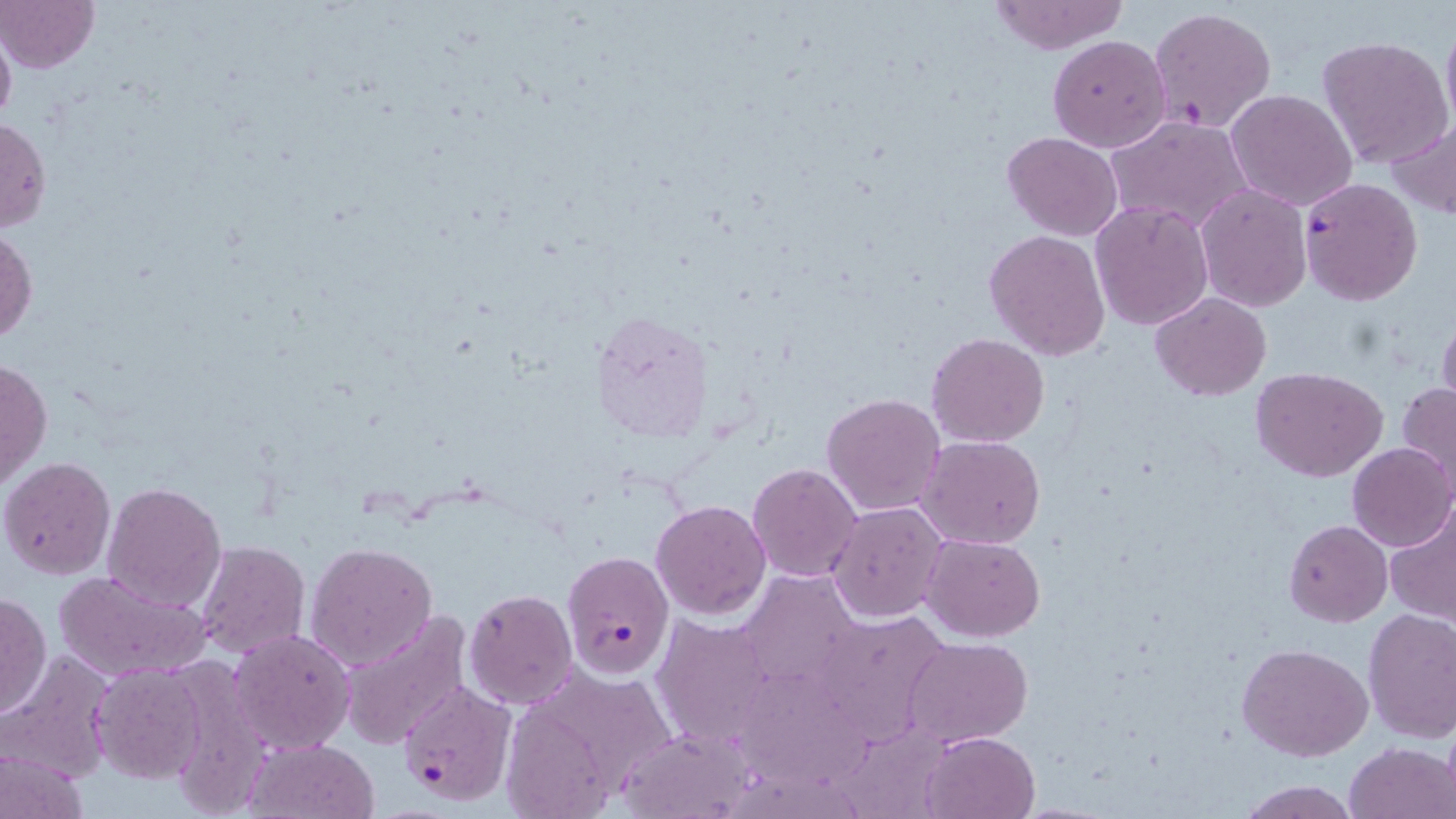

Approximate bounding boxes as (x1, y1, x2, y2) in pixels. Plasmodium falciparum-infected red blood cell locations: (1297, 177, 1422, 305), (562, 549, 675, 680), (396, 681, 519, 806). Uninfected red blood cell locations: (0, 0, 99, 72), (987, 1, 1129, 54), (1148, 7, 1276, 136), (1440, 9, 1456, 138), (0, 17, 16, 138), (1048, 34, 1171, 154), (1317, 35, 1453, 170), (1228, 89, 1357, 212), (1104, 116, 1252, 235), (0, 117, 52, 235), (1388, 117, 1456, 220), (1002, 131, 1124, 239), (1195, 185, 1312, 312), (1090, 201, 1213, 330), (1, 227, 38, 346), (984, 228, 1111, 363), (1150, 291, 1272, 402), (1437, 308, 1456, 422), (590, 312, 709, 443), (926, 333, 1050, 447), (1, 356, 52, 491), (1251, 367, 1388, 481), (1397, 382, 1456, 500), (821, 392, 946, 515), (918, 436, 1047, 550), (1346, 442, 1455, 553), (1, 456, 116, 580), (747, 463, 862, 583), (101, 481, 228, 614), (652, 499, 771, 620), (828, 502, 947, 621), (1383, 502, 1456, 628), (1285, 519, 1393, 626), (923, 533, 1045, 641), (305, 540, 437, 670), (194, 541, 309, 661), (51, 569, 213, 684), (745, 576, 859, 694), (463, 589, 578, 710), (0, 592, 50, 720), (822, 606, 944, 731), (1362, 609, 1456, 741), (336, 610, 472, 749), (652, 616, 779, 748), (228, 629, 358, 756), (905, 637, 1033, 748), (1236, 643, 1375, 762), (0, 652, 116, 783), (90, 664, 209, 784), (542, 672, 682, 780), (740, 676, 874, 790), (503, 705, 619, 819), (846, 719, 940, 814), (613, 721, 763, 819), (920, 731, 1040, 819), (248, 738, 380, 818), (1343, 741, 1455, 819), (1, 744, 89, 819), (735, 767, 865, 819), (1238, 780, 1360, 818). Slide-level diagnosis: Plasmodium falciparum. May-Grünwald-Giemsa stain. Light microscopy. One field of a larger specimen. Image is 1456×819 pixels. Captured at 1000x magnification. Thin blood film.